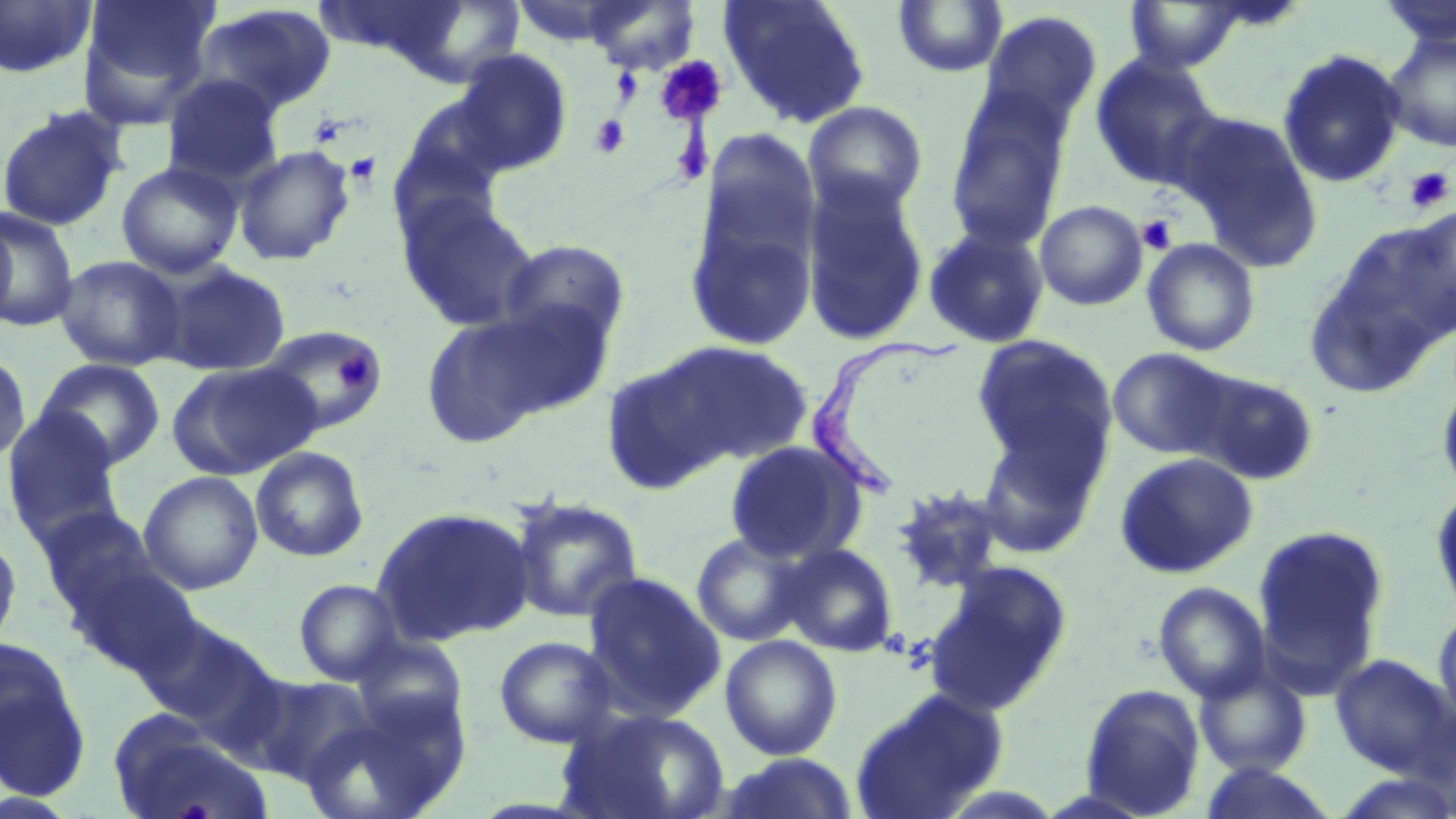
Summary:
  - Coordinate format: approximate bounding boxes as [x1, y1, x2, y2] in pixels
  - Platelet locations: [654, 56, 726, 127], [589, 115, 631, 159], [344, 151, 383, 188], [1404, 167, 1454, 213], [1136, 214, 1178, 254], [335, 354, 375, 392]
  - Uninfected red blood cell locations: [78, 0, 219, 123], [585, 0, 700, 74], [718, 0, 872, 129], [1378, 0, 1456, 48], [0, 1, 97, 79], [893, 1, 1008, 78], [1123, 1, 1251, 73], [192, 3, 338, 118], [981, 10, 1102, 132], [1382, 32, 1456, 152], [1277, 49, 1406, 188], [451, 50, 572, 176], [1090, 54, 1225, 190], [161, 74, 285, 190], [944, 88, 1074, 251], [395, 91, 513, 213], [802, 101, 930, 219], [0, 106, 128, 232], [1174, 109, 1325, 271], [693, 126, 822, 287], [233, 144, 356, 265], [116, 161, 243, 279], [800, 177, 930, 346], [395, 192, 542, 333], [1035, 200, 1148, 311], [0, 206, 79, 331], [1400, 206, 1455, 332], [685, 211, 818, 353], [0, 214, 16, 329], [1332, 219, 1455, 351], [923, 224, 1050, 348], [1142, 237, 1261, 356], [499, 239, 630, 352], [1302, 248, 1445, 400], [54, 255, 186, 371], [152, 261, 291, 377], [475, 299, 619, 419], [421, 314, 554, 449], [258, 325, 388, 436], [971, 333, 1118, 488], [636, 340, 813, 472], [1107, 346, 1240, 461], [0, 349, 31, 465], [36, 358, 166, 471], [167, 361, 322, 481], [1191, 369, 1320, 487], [1434, 372, 1456, 502], [2, 407, 124, 540], [974, 424, 1103, 561], [724, 440, 868, 564], [249, 446, 370, 563], [1115, 451, 1258, 579], [138, 470, 263, 595], [890, 483, 1011, 595], [1429, 485, 1456, 625], [508, 495, 644, 623], [36, 506, 162, 621], [371, 506, 536, 647], [1252, 525, 1389, 691], [0, 531, 23, 654], [690, 531, 811, 646], [780, 543, 900, 657], [67, 560, 202, 678], [923, 561, 1074, 716], [581, 571, 726, 722], [293, 579, 406, 685], [1153, 581, 1271, 703], [1432, 607, 1456, 737], [138, 616, 284, 747], [720, 634, 843, 760], [493, 635, 618, 748], [0, 638, 91, 796], [1329, 652, 1454, 775], [1194, 664, 1312, 777], [236, 670, 377, 787], [1078, 682, 1206, 817], [850, 688, 1009, 819], [556, 705, 730, 819], [108, 715, 269, 819], [715, 753, 861, 819], [1195, 761, 1342, 819]
  - Trypanosoma brucei locations: [804, 337, 971, 503]
  - Slide-level diagnosis: Trypanosoma brucei
  - Image size: 1456×819 pixels
  - Field of view: one of a larger specimen
  - Modality: light microscopy
  - Preparation: thin blood film
  - Stain: May-Grünwald-Giemsa
  - Magnification: 1000x